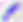

identification: Toxoplasma gondii
magnification: 400x
modality: photomicrograph